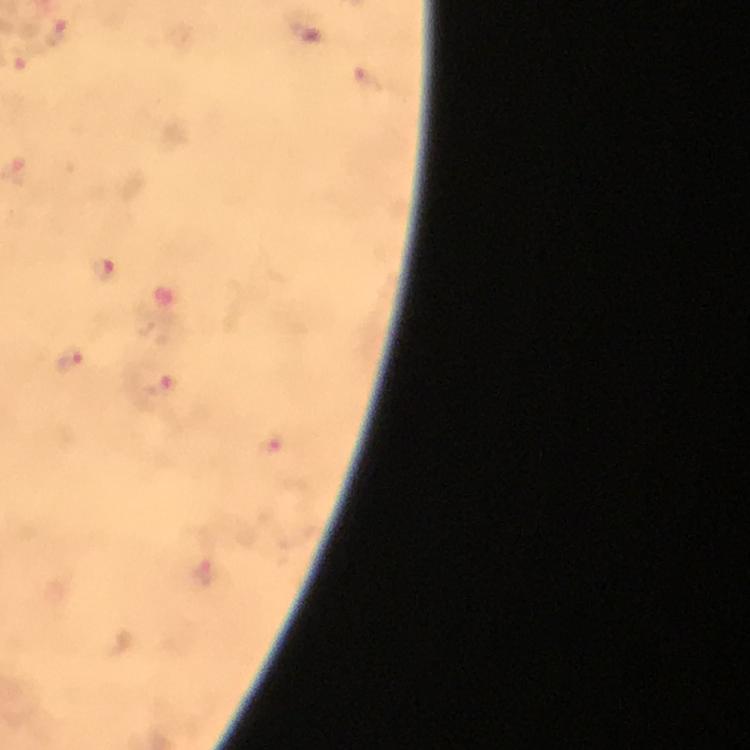
Approximate centers as [x, y] in pixels. Plasmodium parasite locations: [307, 32], [56, 34], [102, 269], [72, 359], [158, 388], [272, 445], [205, 572]. 100x magnification. Giemsa-stained preparation. Thick blood film. Image is 750×750 pixels. Cropped region of a single field of view. Immersion oil was used. From a malaria diagnostic workup. Photographed through the microscope with a smartphone camera.